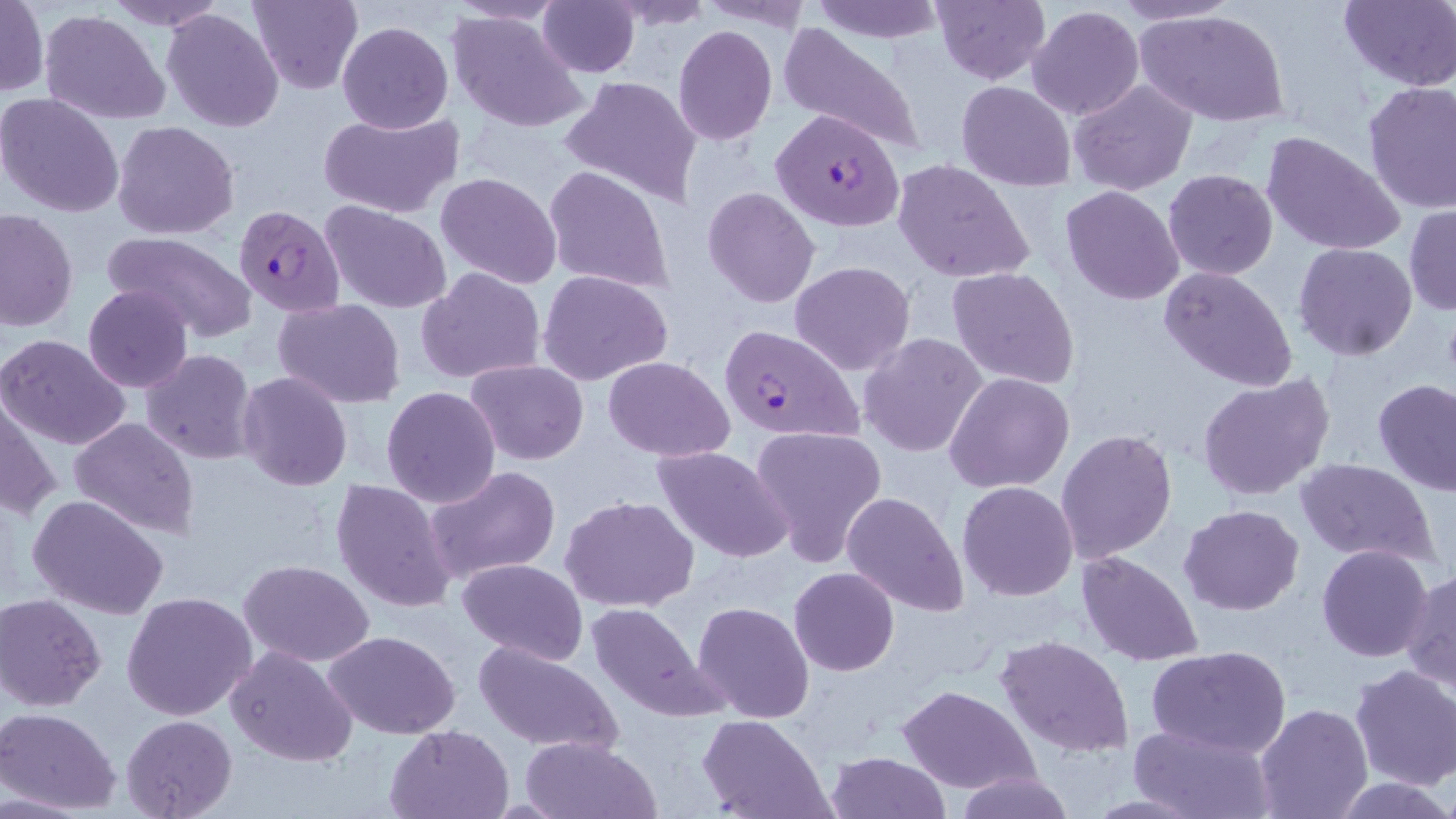

slide_level_diagnosis: Plasmodium falciparum
preparation: thin blood smear
stain: May-Grünwald-Giemsa
uninfected_red_blood_cell_locations: 'approximate bounding boxes as named x1/y1/x2/y2 corners in pixels: (x1=104, y1=0, x2=229, y2=30), (x1=248, y1=0, x2=363, y2=92), (x1=700, y1=0, x2=816, y2=32), (x1=810, y1=0, x2=946, y2=43), (x1=932, y1=0, x2=1049, y2=84), (x1=1112, y1=0, x2=1242, y2=27), (x1=1, y1=1, x2=48, y2=96), (x1=537, y1=1, x2=639, y2=77), (x1=608, y1=1, x2=713, y2=30), (x1=1338, y1=1, x2=1456, y2=90), (x1=1027, y1=5, x2=1145, y2=119), (x1=162, y1=7, x2=284, y2=132), (x1=1135, y1=9, x2=1291, y2=128), (x1=39, y1=10, x2=169, y2=124), (x1=446, y1=10, x2=588, y2=133), (x1=337, y1=22, x2=453, y2=133), (x1=777, y1=23, x2=927, y2=156), (x1=673, y1=24, x2=778, y2=146), (x1=558, y1=75, x2=702, y2=208), (x1=1069, y1=79, x2=1197, y2=196), (x1=956, y1=80, x2=1077, y2=192), (x1=1362, y1=80, x2=1456, y2=213), (x1=0, y1=92, x2=125, y2=219), (x1=317, y1=109, x2=464, y2=220), (x1=112, y1=120, x2=240, y2=239), (x1=1261, y1=130, x2=1405, y2=257), (x1=892, y1=159, x2=1034, y2=284), (x1=543, y1=164, x2=673, y2=296), (x1=1163, y1=169, x2=1279, y2=281), (x1=436, y1=172, x2=562, y2=290), (x1=1061, y1=186, x2=1184, y2=304), (x1=701, y1=187, x2=822, y2=309), (x1=322, y1=202, x2=452, y2=314), (x1=1404, y1=204, x2=1456, y2=315), (x1=0, y1=208, x2=78, y2=332), (x1=102, y1=232, x2=257, y2=345), (x1=1293, y1=243, x2=1418, y2=362), (x1=788, y1=260, x2=915, y2=375), (x1=415, y1=266, x2=547, y2=385), (x1=948, y1=266, x2=1080, y2=390), (x1=1160, y1=266, x2=1297, y2=392), (x1=538, y1=270, x2=675, y2=385), (x1=83, y1=284, x2=194, y2=393), (x1=273, y1=299, x2=405, y2=406), (x1=858, y1=333, x2=989, y2=459), (x1=0, y1=334, x2=131, y2=453), (x1=138, y1=349, x2=259, y2=464), (x1=603, y1=356, x2=734, y2=458), (x1=465, y1=359, x2=589, y2=464), (x1=238, y1=371, x2=353, y2=492), (x1=945, y1=372, x2=1076, y2=493), (x1=1196, y1=374, x2=1336, y2=502), (x1=1372, y1=378, x2=1455, y2=497), (x1=1, y1=385, x2=62, y2=527), (x1=380, y1=386, x2=501, y2=509), (x1=69, y1=417, x2=199, y2=538), (x1=748, y1=423, x2=889, y2=565), (x1=1054, y1=428, x2=1179, y2=563), (x1=652, y1=446, x2=794, y2=564), (x1=1293, y1=458, x2=1442, y2=567), (x1=426, y1=465, x2=561, y2=583), (x1=331, y1=479, x2=458, y2=613), (x1=956, y1=481, x2=1079, y2=601), (x1=840, y1=490, x2=970, y2=617), (x1=26, y1=494, x2=170, y2=622), (x1=559, y1=495, x2=700, y2=612), (x1=1179, y1=503, x2=1305, y2=615), (x1=1316, y1=545, x2=1435, y2=663), (x1=1077, y1=550, x2=1203, y2=666), (x1=456, y1=558, x2=588, y2=666), (x1=239, y1=560, x2=375, y2=667), (x1=790, y1=567, x2=899, y2=676), (x1=1403, y1=569, x2=1455, y2=696), (x1=121, y1=590, x2=259, y2=723), (x1=2, y1=593, x2=108, y2=711), (x1=693, y1=600, x2=815, y2=722), (x1=586, y1=601, x2=726, y2=723), (x1=323, y1=630, x2=461, y2=739), (x1=994, y1=634, x2=1135, y2=758), (x1=473, y1=640, x2=624, y2=755), (x1=227, y1=645, x2=357, y2=768), (x1=1146, y1=645, x2=1291, y2=759), (x1=1348, y1=664, x2=1456, y2=790), (x1=897, y1=684, x2=1040, y2=794), (x1=1254, y1=702, x2=1372, y2=819), (x1=1, y1=708, x2=121, y2=814), (x1=120, y1=715, x2=236, y2=818), (x1=700, y1=715, x2=833, y2=819), (x1=384, y1=723, x2=514, y2=818), (x1=1129, y1=725, x2=1272, y2=817), (x1=518, y1=736, x2=660, y2=818), (x1=827, y1=751, x2=947, y2=819), (x1=956, y1=771, x2=1074, y2=819), (x1=1337, y1=778, x2=1452, y2=817)'
image_size: 1456×819 pixels
plasmodium_falciparum_infected_red_blood_cell_locations: 'approximate bounding boxes as named x1/y1/x2/y2 corners in pixels: (x1=771, y1=108, x2=906, y2=232), (x1=233, y1=205, x2=346, y2=316), (x1=718, y1=324, x2=866, y2=446)'
field_of_view: one of a larger specimen
magnification: 1000x
modality: light microscopy